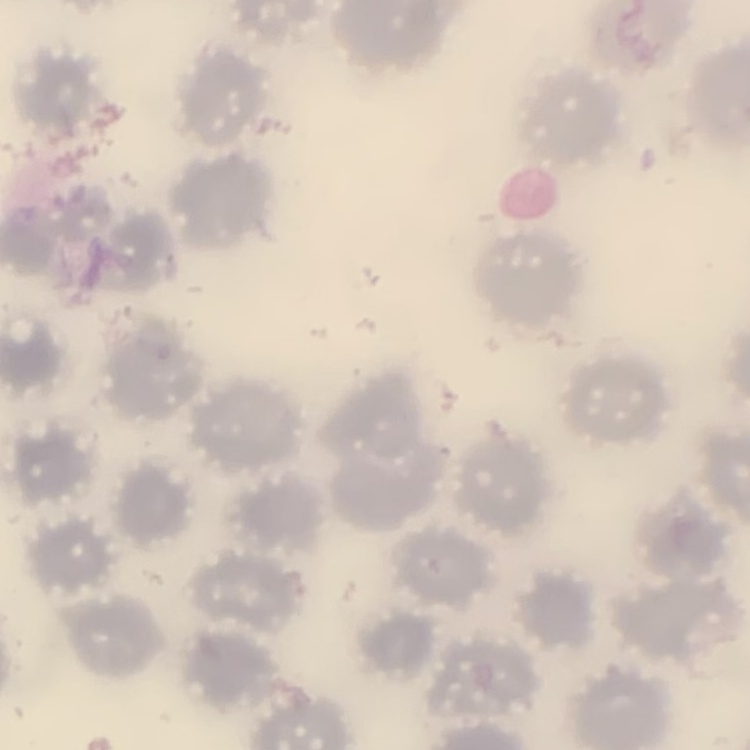 The erythrocytes show no rouleaux formation. Thin blood smear. Square crop of a larger photomicrograph. Stained with either Field's or Giemsa.